Classify this cell by malaria status.
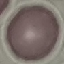
It is uninfected.

Automatically extracted cell patch, resized to 64 × 64 pixels. Photographed with a smartphone camera at the microscope eyepiece. Giemsa stain. Thin blood film.